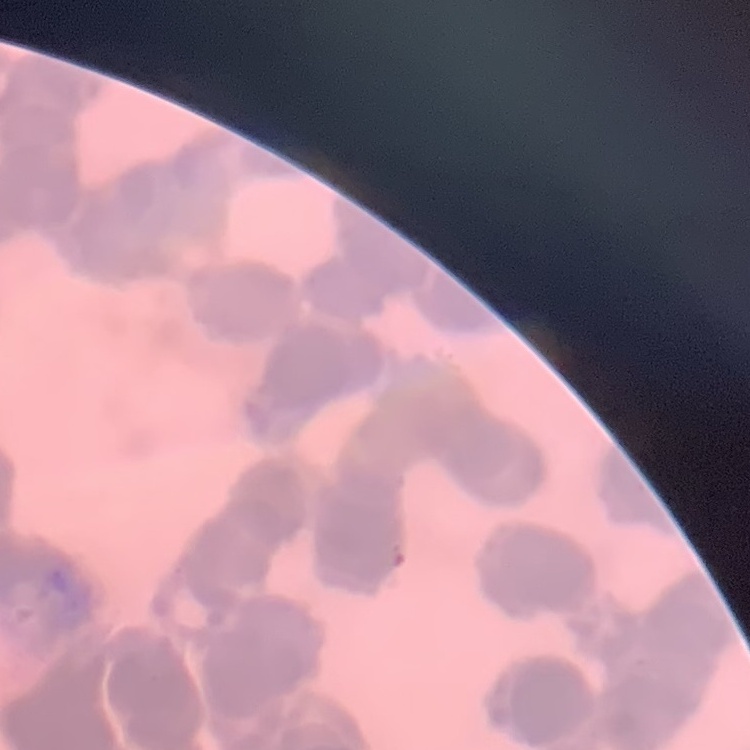

The erythrocytes show rouleaux formation. Thin blood smear. One tile cut from a larger photomicrograph. Stained with either Field's or Giemsa.